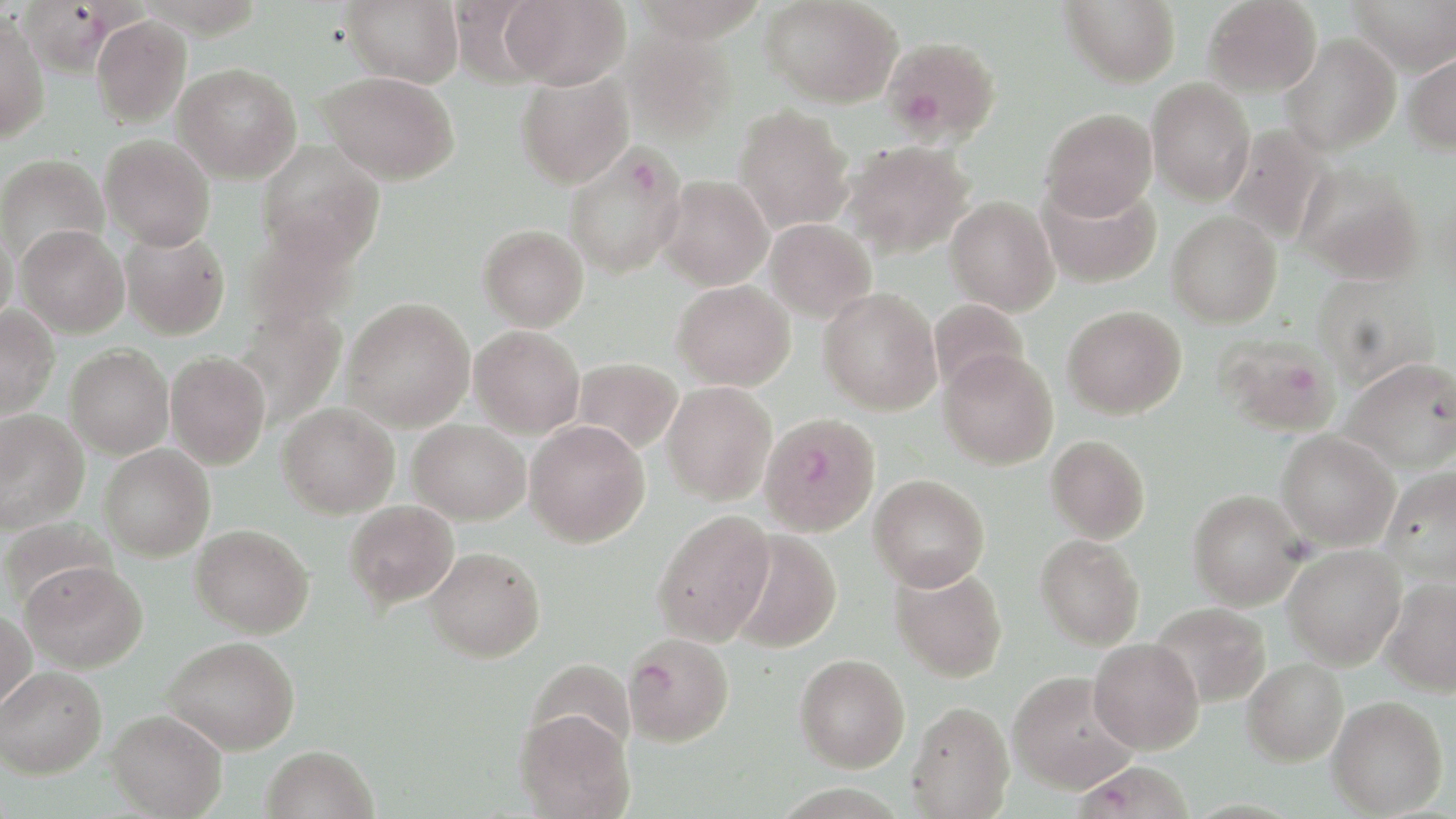

Approximate bounding boxes as (x1, y1, x2, y2) in pixels. Uninfected red blood cell locations: (341, 0, 464, 87), (500, 0, 631, 90), (630, 0, 769, 42), (762, 0, 902, 108), (1061, 0, 1181, 87), (1203, 0, 1322, 97), (1348, 0, 1456, 76), (0, 15, 50, 142), (92, 16, 191, 128), (621, 29, 735, 145), (1281, 33, 1401, 156), (1401, 50, 1456, 154), (172, 62, 302, 183), (515, 70, 635, 189), (319, 71, 460, 185), (1147, 78, 1255, 205), (734, 106, 854, 233), (1040, 108, 1157, 220), (1225, 124, 1332, 246), (99, 134, 215, 251), (841, 140, 976, 258), (256, 142, 385, 267), (0, 154, 109, 265), (1296, 162, 1426, 284), (658, 175, 773, 290), (1037, 177, 1161, 289), (946, 196, 1059, 315), (1167, 210, 1282, 329), (764, 219, 876, 323), (243, 221, 362, 332), (16, 224, 130, 338), (478, 224, 589, 331), (0, 226, 18, 332), (120, 227, 231, 340), (1312, 274, 1442, 390), (673, 280, 795, 391), (818, 287, 942, 414), (342, 297, 475, 432), (929, 298, 1029, 394), (235, 305, 347, 427), (1062, 305, 1187, 419), (0, 306, 59, 419), (469, 325, 585, 439), (65, 344, 174, 459), (938, 349, 1058, 470), (165, 351, 271, 470), (1340, 357, 1456, 473), (573, 358, 683, 454), (662, 382, 777, 504), (278, 402, 400, 519), (0, 409, 89, 533), (408, 419, 530, 525), (525, 420, 650, 548), (1276, 430, 1400, 551), (1046, 435, 1150, 543), (99, 444, 215, 561), (1380, 467, 1456, 584), (869, 474, 990, 591), (1188, 489, 1306, 610), (344, 500, 458, 610), (653, 509, 776, 647), (1, 517, 118, 613), (190, 524, 314, 638), (728, 529, 843, 654), (1035, 534, 1145, 650), (1282, 543, 1406, 669), (424, 546, 545, 662), (21, 561, 148, 673), (890, 565, 1008, 682), (1381, 578, 1456, 696), (1149, 602, 1271, 707), (0, 608, 36, 718), (163, 636, 301, 755), (1088, 639, 1204, 754), (794, 654, 910, 772), (1241, 658, 1347, 766), (526, 659, 636, 760), (1, 665, 107, 779), (1008, 671, 1137, 794), (1328, 695, 1448, 817), (907, 701, 1014, 818), (107, 709, 228, 818), (515, 709, 635, 819), (261, 744, 379, 819). Plasmodium falciparum-infected red blood cell locations: (17, 2, 117, 77), (883, 36, 1000, 144), (562, 142, 688, 280), (1214, 333, 1341, 437), (759, 412, 880, 536), (622, 633, 735, 747), (1073, 760, 1195, 818). Slide-level diagnosis: Plasmodium falciparum. Optical microscopy. Thin blood smear. Single field of view. Image is 1456×819 pixels. Captured at 1000x magnification. May-Grünwald-Giemsa-stained preparation.